Point out each leukocyte.
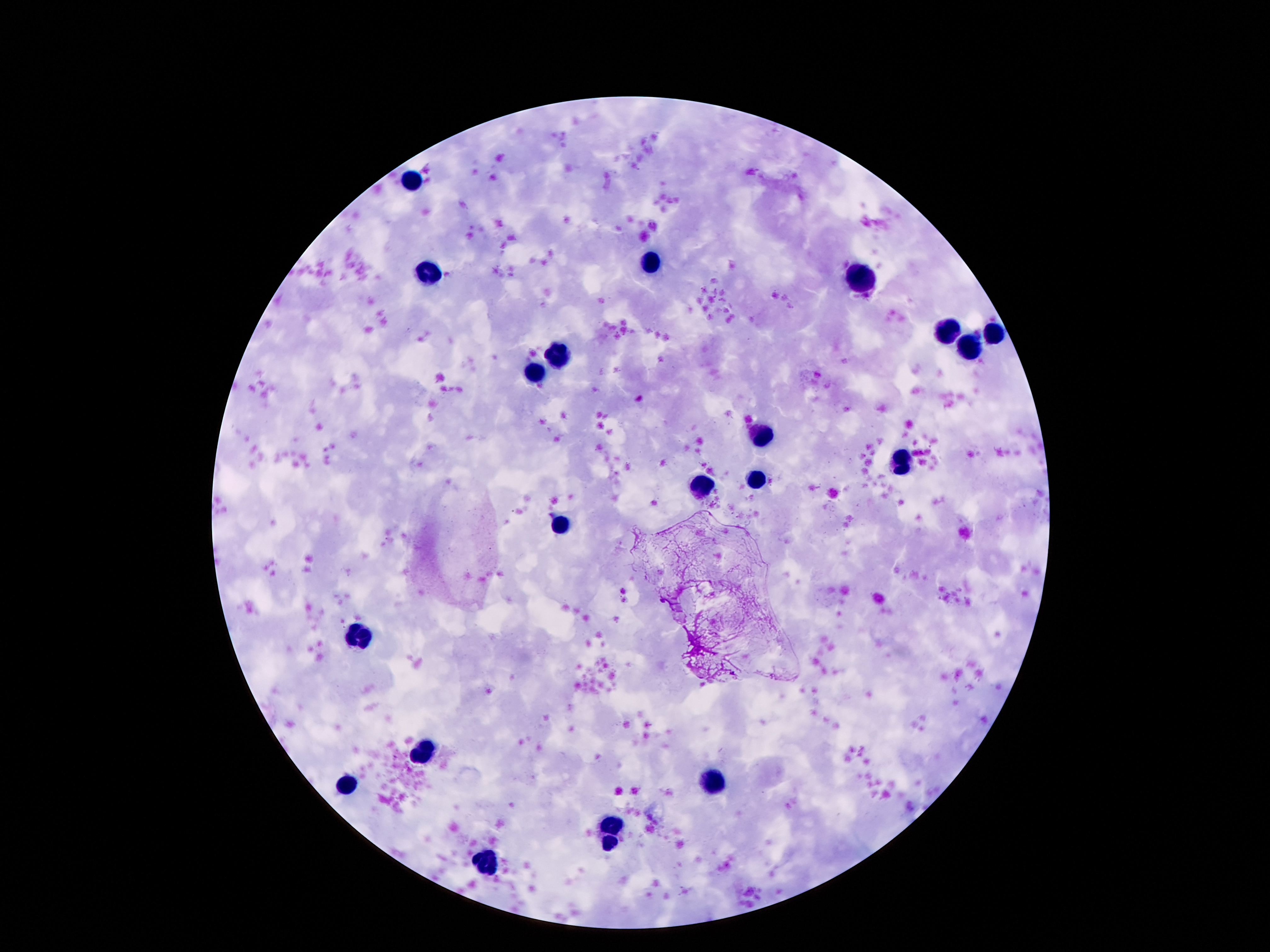
Approximate object centers, in pixels from the top-left corner.
Leukocytes: (x=412, y=181), (x=652, y=262), (x=433, y=277), (x=862, y=279), (x=944, y=331), (x=994, y=333), (x=967, y=348), (x=562, y=354), (x=538, y=373), (x=763, y=434), (x=898, y=461), (x=755, y=479), (x=702, y=490), (x=561, y=526), (x=356, y=631), (x=423, y=750), (x=347, y=785), (x=717, y=787), (x=612, y=825), (x=608, y=843), (x=486, y=864).

Summary:
  - Capture: smartphone camera through the microscope eyepiece
  - Preparation: thick blood smear
  - Patient malaria status: uninfected
  - Field of view: single
  - Stain: Giemsa
  - Image size: 1270×952 pixels
  - Magnification: 100x